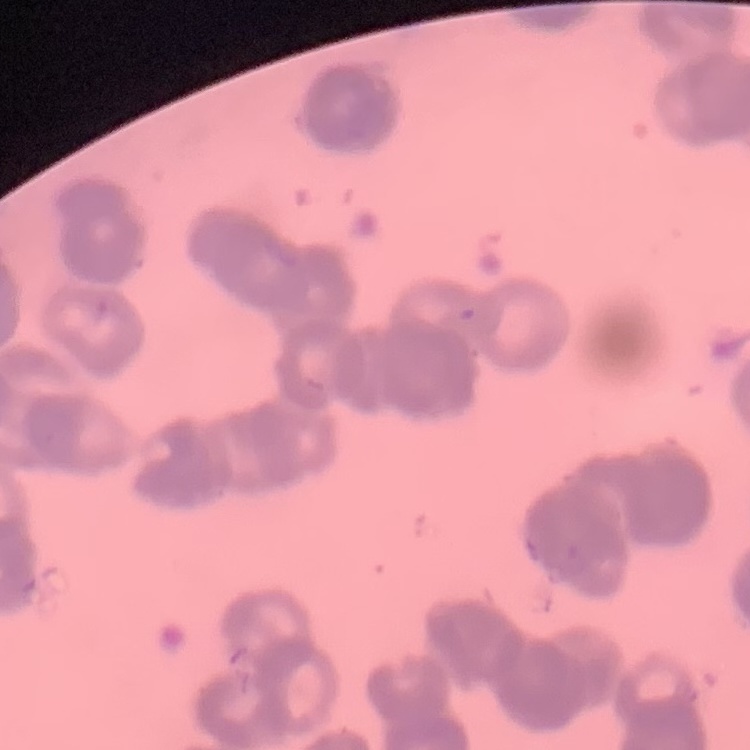

Summary:
  - Red blood cell morphology: rouleaux formation
  - Image type: square crop of a larger photomicrograph
  - Preparation: thin blood film
  - Stain: Field's or Giemsa